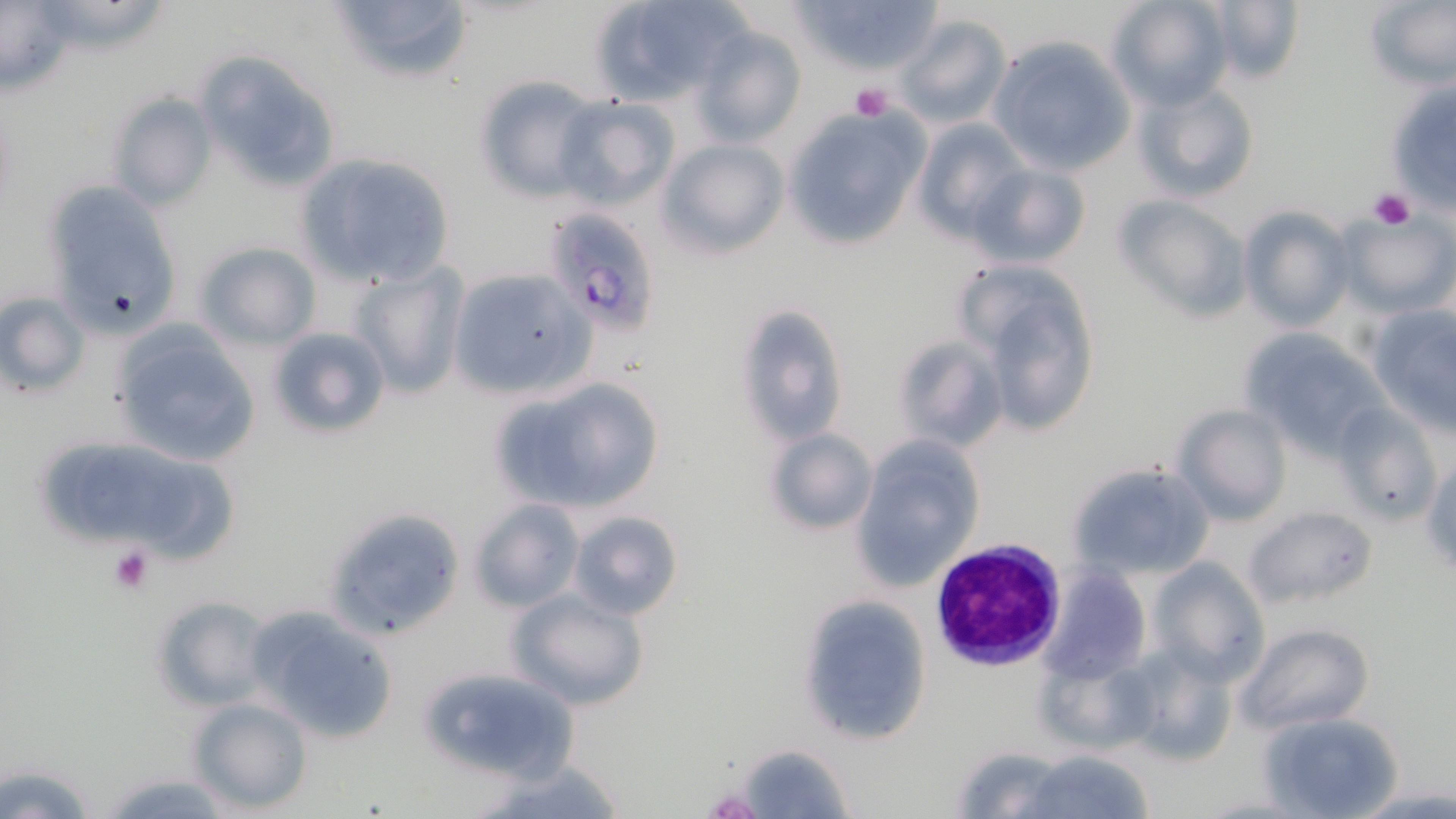

Approximate bounding boxes as (x1,y1)-(x2,y2) corner pairs in pixels. Plasmodium falciparum-infected red blood cell locations: (554,210)-(656,344), (931,538)-(1067,671). Platelet locations: (850,83)-(893,120), (1367,189)-(1414,230), (106,543)-(158,595). Uninfected red blood cell locations: (40,0)-(168,55), (324,0)-(476,86), (587,0)-(751,106), (787,0)-(945,77), (1105,0)-(1234,110), (1362,0)-(1455,91), (1197,1)-(1304,86), (0,2)-(82,100), (894,12)-(1014,129), (690,22)-(807,149), (988,36)-(1136,175), (194,51)-(344,196), (473,77)-(602,203), (1131,77)-(1263,203), (1386,79)-(1456,213), (108,89)-(220,211), (552,97)-(680,210), (786,106)-(931,250), (911,116)-(1029,241), (656,138)-(788,258), (292,152)-(455,289), (970,163)-(1091,268), (41,181)-(185,337), (1111,193)-(1253,323), (1239,206)-(1354,334), (1334,212)-(1456,317), (195,241)-(321,350), (960,262)-(1102,437), (349,264)-(466,399), (445,268)-(597,398), (0,291)-(89,397), (732,304)-(847,446), (1364,305)-(1456,434), (110,326)-(262,468), (265,326)-(392,440), (1237,327)-(1391,458), (892,334)-(1009,454), (488,378)-(665,515), (1171,403)-(1293,525), (1332,403)-(1444,523), (764,428)-(878,535), (850,436)-(985,591), (78,452)-(200,550), (1423,456)-(1455,576), (1065,461)-(1216,582), (469,498)-(584,612), (323,505)-(466,643), (1243,505)-(1376,612), (567,509)-(684,619), (1148,557)-(1269,684), (1040,567)-(1151,683), (505,590)-(649,711), (149,595)-(275,713), (797,595)-(934,747), (247,604)-(402,742), (1235,621)-(1375,735), (1119,642)-(1238,768), (414,666)-(584,785), (185,696)-(314,815), (1259,712)-(1404,819), (734,742)-(856,818), (946,744)-(1071,817), (1019,749)-(1155,819), (477,759)-(629,819), (1,761)-(101,818), (98,773)-(240,817). Slide-level diagnosis: Plasmodium falciparum. 1000x magnification. Image is 1456×819 pixels. Single field of view. Optical microscopy. Thin blood film. May-Grünwald-Giemsa-stained preparation.